Point out each Plasmodium parasite and classify it by life-cycle stage.
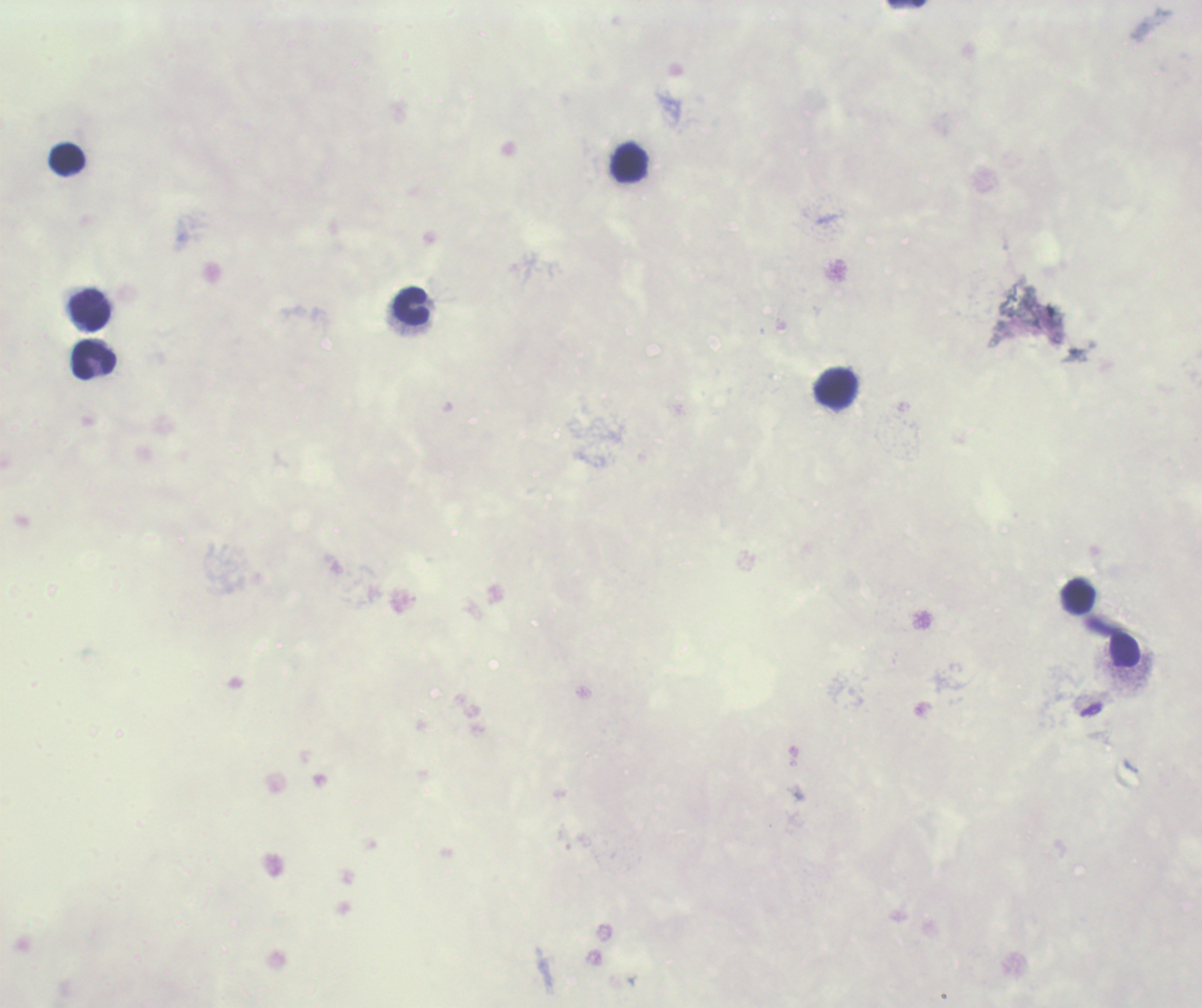

Negative for Plasmodium parasites.

{
  "magnification": "100x",
  "image_size": "1202×1008 pixels",
  "stain": "Romanowsky",
  "field_of_view": "single",
  "context": "previously used in a real diagnosis",
  "leukocyte_locations": "approximate centers as [x, y] in pixels: [68, 159], [630, 163], [411, 305], [90, 310], [95, 360], [836, 389], [1078, 597]",
  "background_quality": "poor",
  "preparation": "thick smear of blood",
  "coloration_quality": "bad"
}